Identify the blood parasite species.
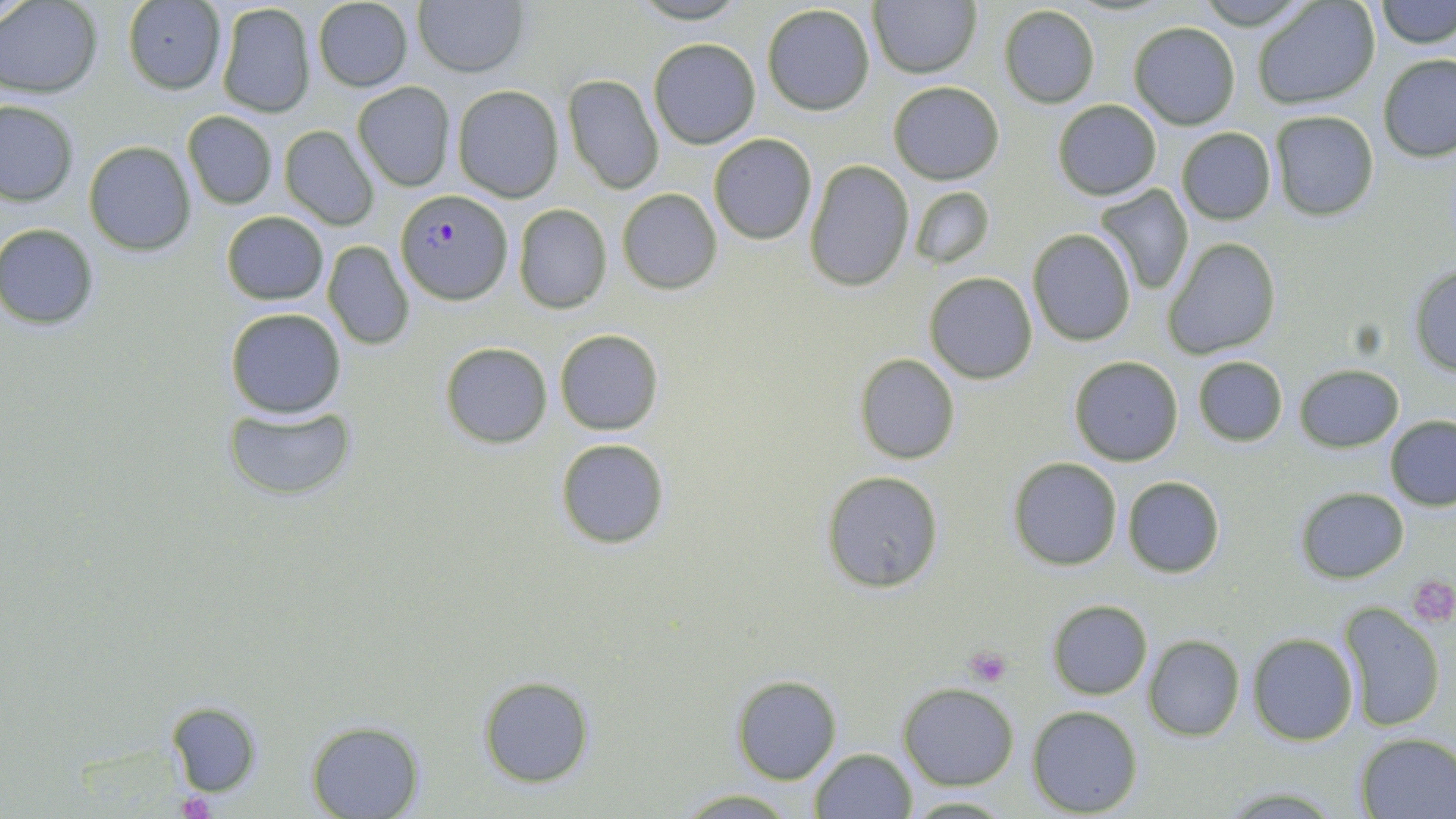
Plasmodium falciparum.

Approximate bounding boxes as (x1,y1)-(x2,y2) corner pairs in pixels. Uninfected red blood cell locations: (631,0)-(751,25), (1193,0)-(1315,31), (1377,0)-(1455,47), (0,1)-(102,98), (123,1)-(226,94), (413,1)-(529,79), (869,1)-(981,78), (1252,1)-(1381,109), (312,2)-(414,92), (215,4)-(315,119), (762,4)-(876,115), (998,5)-(1100,109), (1128,22)-(1242,130), (647,37)-(760,150), (1377,54)-(1456,162), (563,74)-(663,194), (352,81)-(456,192), (887,81)-(1005,184), (453,85)-(565,202), (0,100)-(78,206), (1052,100)-(1161,199), (182,110)-(278,209), (1268,111)-(1379,222), (280,125)-(379,230), (1175,128)-(1276,225), (708,134)-(818,244), (82,140)-(197,255), (804,160)-(915,291), (1094,183)-(1194,297), (908,186)-(993,269), (617,188)-(722,294), (512,204)-(612,314), (221,211)-(329,304), (1,222)-(100,328), (1027,230)-(1136,347), (1165,238)-(1281,359), (322,241)-(415,349), (1408,263)-(1456,377), (925,273)-(1038,384), (225,308)-(346,419), (554,329)-(663,435), (440,342)-(552,448), (854,352)-(960,464), (1068,356)-(1183,466), (1193,356)-(1288,447), (1296,365)-(1404,451), (223,405)-(355,499), (1384,416)-(1456,510), (553,436)-(669,550), (1008,457)-(1122,570), (820,469)-(944,592), (1122,476)-(1224,577), (1294,485)-(1410,583), (1048,600)-(1151,697), (1336,605)-(1446,732), (1246,633)-(1359,746), (1144,636)-(1244,741), (730,674)-(842,785), (477,676)-(594,788), (899,684)-(1018,788), (163,700)-(262,798), (1028,705)-(1143,817), (306,720)-(426,819), (1354,732)-(1456,818), (809,747)-(916,818), (673,790)-(803,818), (902,794)-(1017,817). Platelet locations: (1409,573)-(1456,624), (963,646)-(1012,688), (176,789)-(215,818). Plasmodium falciparum-infected red blood cell locations: (395,189)-(511,303). Image is 1456×819 pixels. Captured at 1000x magnification. May-Grünwald-Giemsa stain. Thin blood smear. Single field of view. Light microscopy.